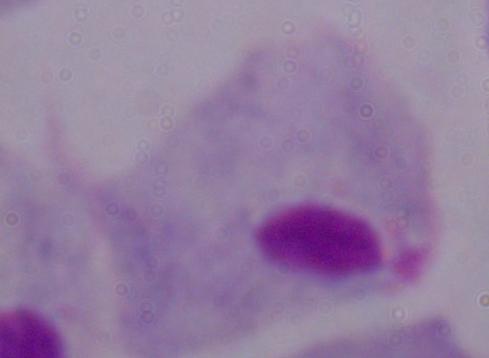

magnification = 1000x
modality = photomicrograph
identification = trichomonad